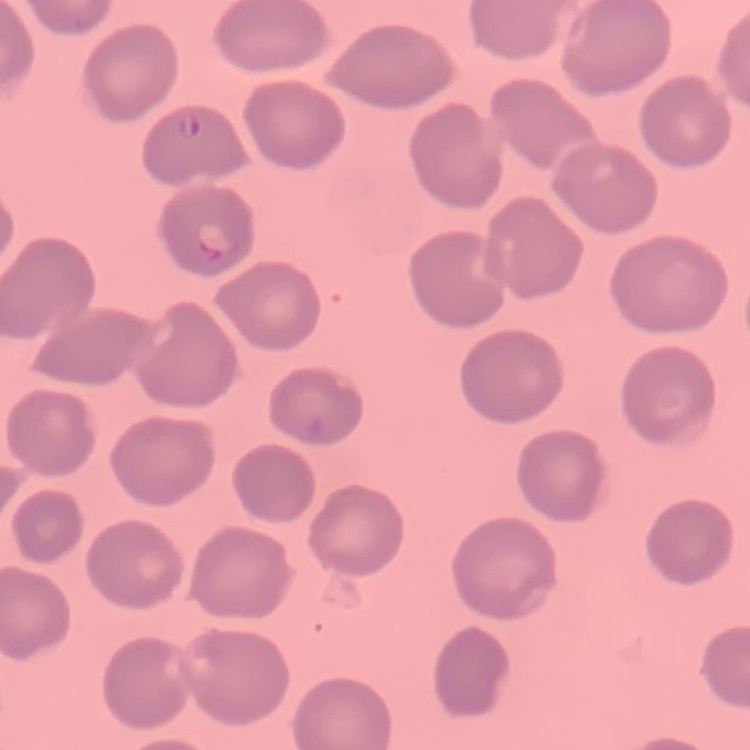 The red blood cells show no rouleaux formation. Field's or Giemsa stain. Thin blood smear. Square crop of a larger photomicrograph.